Locate leukocytes (white blood cells).
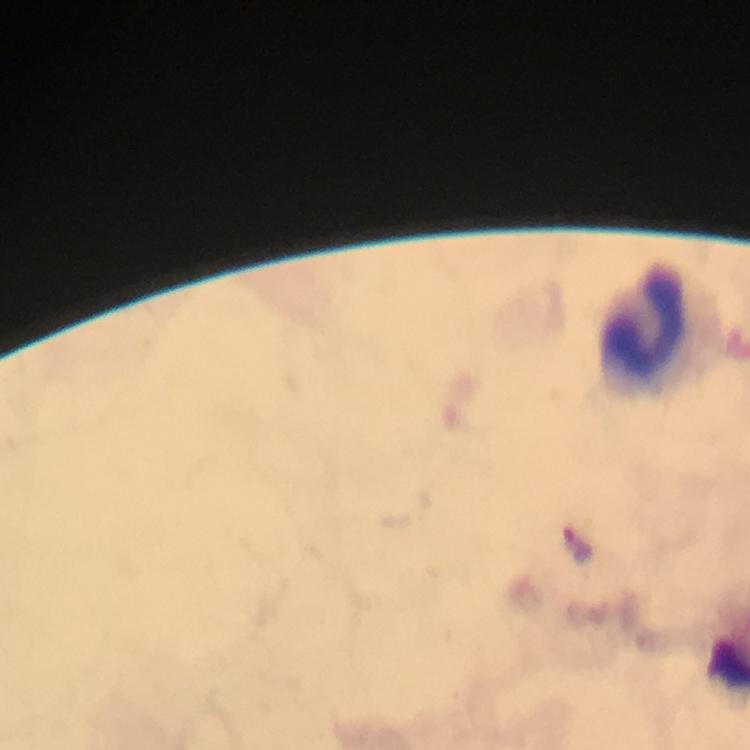
Approximate centers as [x, y] in pixels.
Leukocytes: [645, 327].

context: from a malaria diagnostic workup
capture: smartphone mounted on the microscope
stain: Giemsa
plasmodium_parasite_locations: 'approximate centers as [x, y] in pixels: [577, 542]'
immersion_oil: applied
preparation: thick blood film
magnification: 100x
image_size: 750×750 pixels
cropped_from: one field of view